Assess the morphology of the red blood cells.
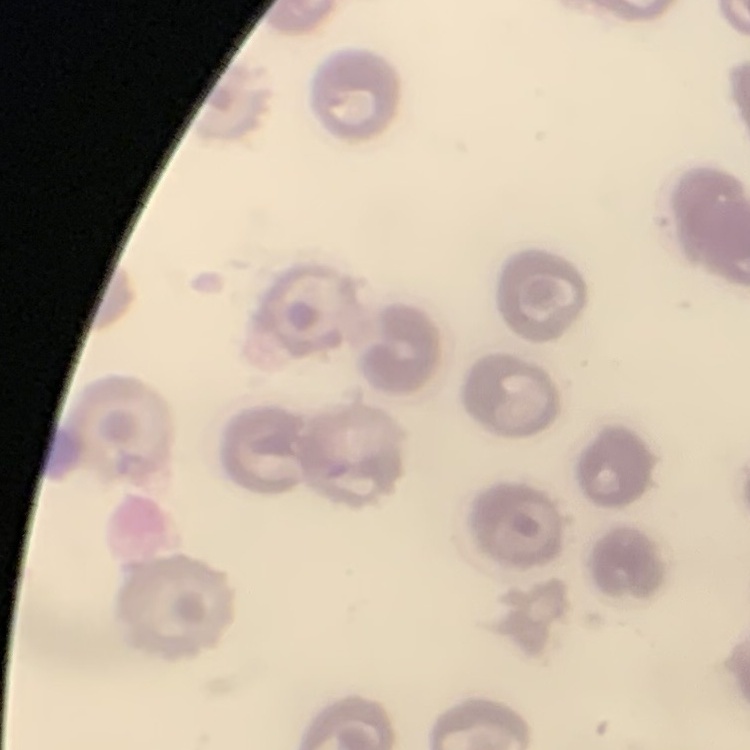
They show no rouleaux formation.

One tile cut from a larger photomicrograph. Thin blood smear. Field's or Giemsa stain.